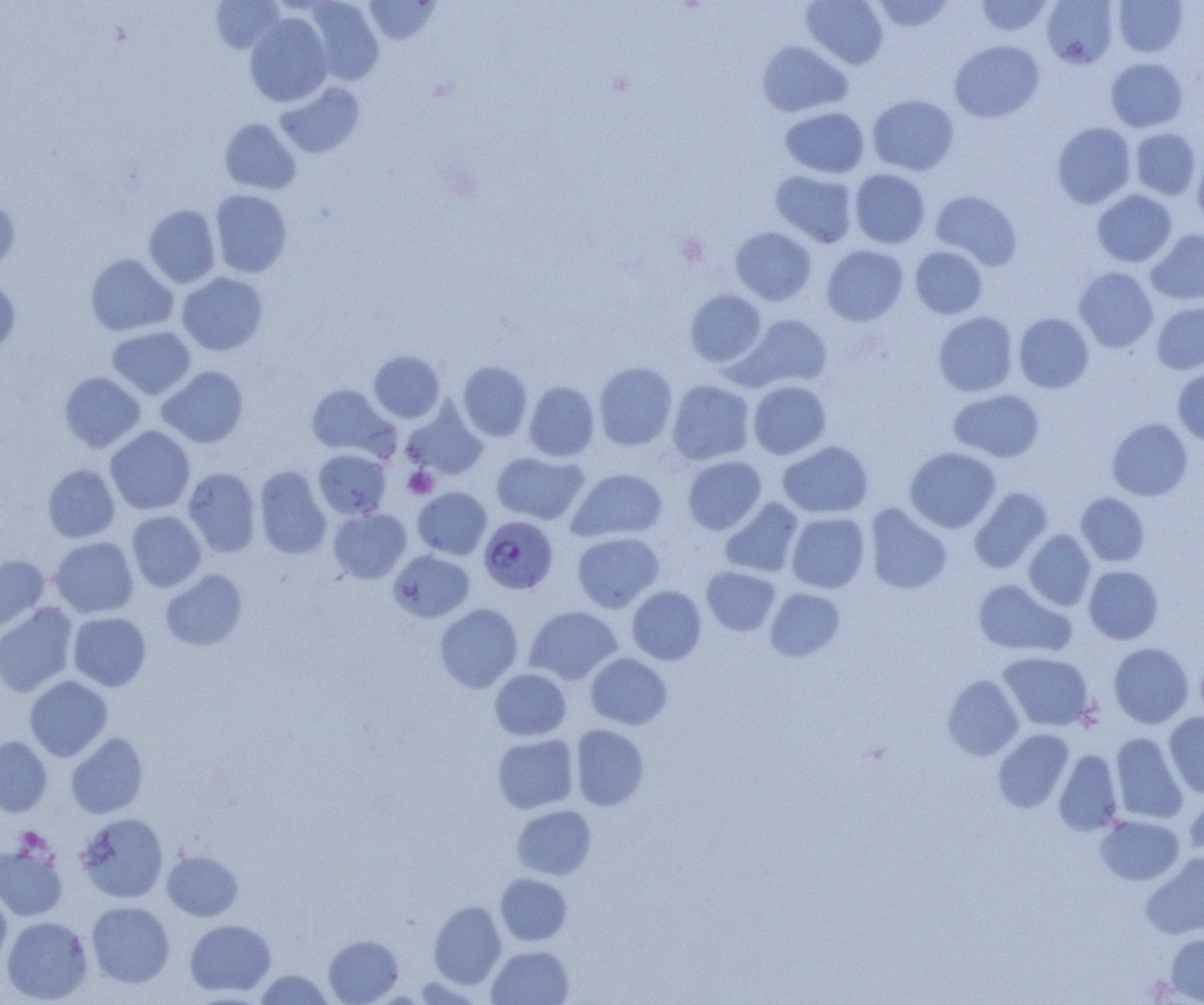
Summary:
  - Coordinate format: approximate bounding boxes as [x1, y1, x2, y2] in pixels
  - Platelet locations: [403, 466, 438, 498]
  - Uninfected red blood cell locations: [210, 0, 284, 54], [304, 0, 384, 85], [364, 0, 440, 45], [801, 0, 889, 68], [975, 0, 1053, 37], [1040, 0, 1119, 68], [871, 1, 955, 33], [1112, 1, 1188, 57], [244, 12, 333, 107], [949, 39, 1045, 122], [757, 41, 852, 117], [1106, 57, 1188, 132], [276, 81, 365, 158], [867, 94, 959, 175], [780, 106, 870, 178], [220, 118, 301, 194], [1052, 122, 1136, 208], [1130, 128, 1202, 200], [1192, 149, 1204, 230], [850, 169, 930, 248], [770, 170, 858, 248], [210, 189, 293, 277], [930, 189, 1023, 270], [1092, 190, 1177, 267], [0, 193, 20, 272], [143, 204, 221, 287], [730, 226, 816, 305], [1146, 229, 1204, 305], [821, 245, 908, 326], [910, 246, 987, 319], [85, 253, 178, 335], [1073, 267, 1158, 353], [176, 272, 268, 355], [0, 277, 21, 355], [685, 289, 766, 367], [1151, 301, 1204, 375], [933, 311, 1018, 396], [1014, 313, 1094, 393], [739, 314, 833, 390], [107, 326, 196, 399], [369, 350, 445, 423], [458, 361, 532, 441], [594, 361, 678, 450], [156, 365, 248, 448], [1172, 368, 1204, 446], [59, 371, 146, 452], [667, 379, 755, 464], [748, 380, 832, 459], [523, 381, 599, 461], [306, 383, 396, 460], [949, 389, 1045, 462], [402, 404, 488, 480], [1107, 418, 1193, 501], [105, 425, 195, 514], [777, 440, 873, 518], [905, 447, 1001, 533], [313, 449, 391, 519], [491, 451, 588, 524], [682, 456, 766, 534], [42, 464, 120, 542], [254, 466, 332, 559], [182, 467, 262, 558], [567, 468, 668, 543], [412, 487, 492, 560], [968, 487, 1053, 573], [1075, 492, 1150, 566], [720, 498, 803, 578], [864, 503, 953, 594], [328, 508, 411, 583], [126, 511, 207, 591], [786, 512, 870, 593], [1024, 529, 1095, 610], [572, 531, 664, 612], [50, 536, 139, 618], [389, 550, 475, 623], [0, 555, 50, 633], [1084, 565, 1164, 643], [701, 566, 781, 636], [160, 569, 248, 651], [972, 579, 1075, 657], [627, 586, 707, 664], [765, 588, 845, 661], [0, 603, 77, 697], [434, 603, 523, 692], [525, 606, 622, 684], [67, 612, 151, 691], [1108, 642, 1194, 728], [585, 652, 672, 730], [998, 652, 1094, 731], [489, 668, 571, 740], [942, 675, 1024, 760], [24, 676, 112, 761], [1165, 712, 1204, 798], [570, 724, 650, 811], [993, 729, 1074, 812], [66, 732, 149, 819], [1110, 733, 1188, 824], [492, 734, 578, 813], [0, 736, 52, 817], [1054, 750, 1123, 836], [1184, 794, 1204, 860], [512, 805, 597, 880], [76, 813, 169, 903], [1095, 814, 1185, 886], [0, 845, 68, 920], [162, 849, 243, 921], [1141, 853, 1204, 939], [495, 874, 572, 945], [0, 888, 11, 968], [86, 901, 175, 987], [428, 901, 506, 988], [1, 916, 93, 1004], [184, 919, 276, 996], [1166, 933, 1204, 1003], [323, 934, 404, 1004], [487, 945, 573, 1005], [254, 969, 333, 1004]
  - Plasmodium falciparum-infected red blood cell locations: [478, 516, 558, 594]
  - Slide-level diagnosis: Plasmodium falciparum
  - Modality: light microscopy
  - Magnification: 1000x
  - Image size: 1204×1005 pixels
  - Field of view: single
  - Preparation: thin blood smear